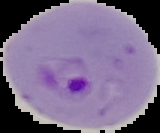
Summary:
  - Image size: 160×133 pixels
  - Image type: segmented cell region on a black background
  - Result: malaria parasites identified
  - Preparation: thin blood smear